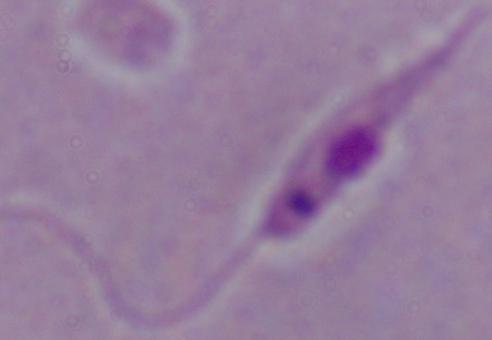 A Leishmania parasite is seen. Photomicrograph. Captured at 1000x magnification.